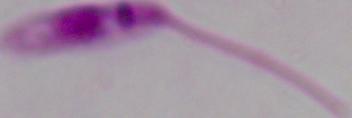
{
  "magnification": "1000x",
  "identification": "Leishmania",
  "modality": "micrograph"
}